Give the extent of all Plasmodium vivax-infected red blood cells.
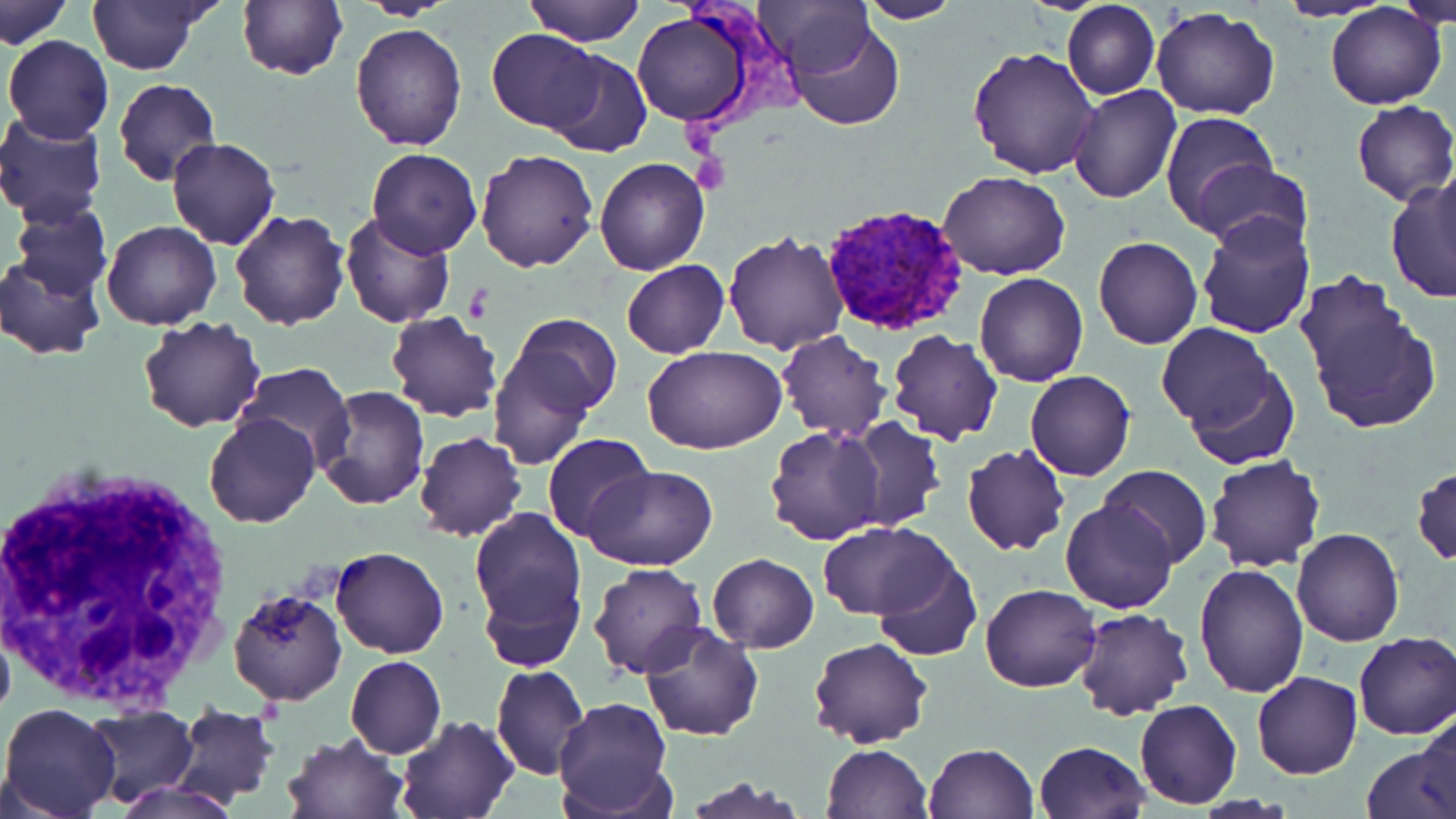
Approximate bounding boxes as (x1, y1, x2, y2) in pixels.
Plasmodium vivax-infected red blood cells: (820, 206, 971, 337).

slide-level diagnosis = Plasmodium vivax
modality = light microscopy
image size = 1456×819 pixels
white blood cell locations = approximate bounding boxes as (x1, y1, x2, y2) in pixels: (1, 461, 241, 709)
platelet locations = approximate bounding boxes as (x1, y1, x2, y2) in pixels: (464, 284, 494, 323)
field of view = single
uninfected red blood cell locations = approximate bounding boxes as (x1, y1, x2, y2) in pixels: (87, 0, 212, 74), (237, 0, 348, 82), (523, 0, 645, 47), (758, 0, 876, 76), (1276, 0, 1391, 22), (1394, 0, 1456, 27), (1, 1, 71, 49), (857, 1, 964, 24), (1061, 1, 1160, 99), (1326, 4, 1447, 110), (1151, 7, 1278, 120), (630, 10, 755, 127), (785, 20, 907, 132), (351, 25, 467, 150), (487, 28, 604, 130), (4, 35, 114, 143), (967, 45, 1098, 178), (543, 50, 652, 158), (113, 77, 222, 187), (1067, 84, 1181, 203), (1352, 101, 1456, 207), (1160, 110, 1282, 232), (0, 112, 108, 222), (167, 137, 279, 251), (367, 148, 481, 259), (475, 149, 600, 272), (594, 157, 708, 274), (1194, 158, 1312, 254), (1435, 161, 1455, 279), (206, 165, 327, 302), (939, 169, 1070, 280), (1386, 177, 1456, 303), (6, 199, 113, 299), (229, 209, 349, 330), (1193, 209, 1316, 338), (339, 212, 455, 329), (102, 220, 220, 329), (723, 230, 850, 353), (1093, 236, 1203, 350), (0, 252, 107, 360), (622, 260, 730, 358), (976, 272, 1087, 387), (1297, 274, 1440, 435), (385, 311, 504, 422), (502, 314, 623, 429), (138, 316, 266, 432), (1156, 323, 1274, 430), (886, 330, 1003, 445), (776, 331, 890, 442), (488, 346, 599, 473), (643, 347, 787, 455), (232, 362, 355, 467), (1183, 364, 1300, 472), (1024, 369, 1135, 482), (314, 386, 430, 510), (203, 412, 320, 529), (839, 417, 945, 532), (766, 426, 886, 545), (413, 432, 526, 542), (544, 434, 651, 541), (963, 443, 1069, 556), (1205, 454, 1325, 573), (1099, 463, 1212, 567), (581, 464, 719, 568), (1413, 466, 1456, 566), (1062, 498, 1178, 614), (468, 508, 588, 643), (819, 520, 952, 620), (1292, 528, 1405, 646), (331, 547, 449, 659), (707, 553, 818, 652), (871, 555, 982, 661), (589, 563, 706, 677), (1192, 564, 1309, 699), (479, 575, 584, 673), (980, 583, 1101, 692), (228, 588, 347, 707), (1076, 607, 1192, 719), (640, 623, 763, 741), (1353, 631, 1455, 740), (807, 638, 931, 749), (344, 654, 447, 758), (492, 665, 589, 781), (1252, 672, 1362, 778), (553, 696, 672, 818), (1134, 698, 1241, 809), (1, 703, 122, 818), (170, 705, 281, 805), (81, 707, 197, 804), (1411, 712, 1454, 816), (395, 714, 518, 819), (283, 732, 408, 818), (1033, 740, 1151, 819), (1362, 742, 1454, 819), (820, 743, 932, 818), (922, 743, 1038, 819), (683, 776, 811, 817), (112, 781, 236, 819)
preparation = thin blood smear
stain = May-Grünwald-Giemsa
magnification = 1000x